State the preparation type.
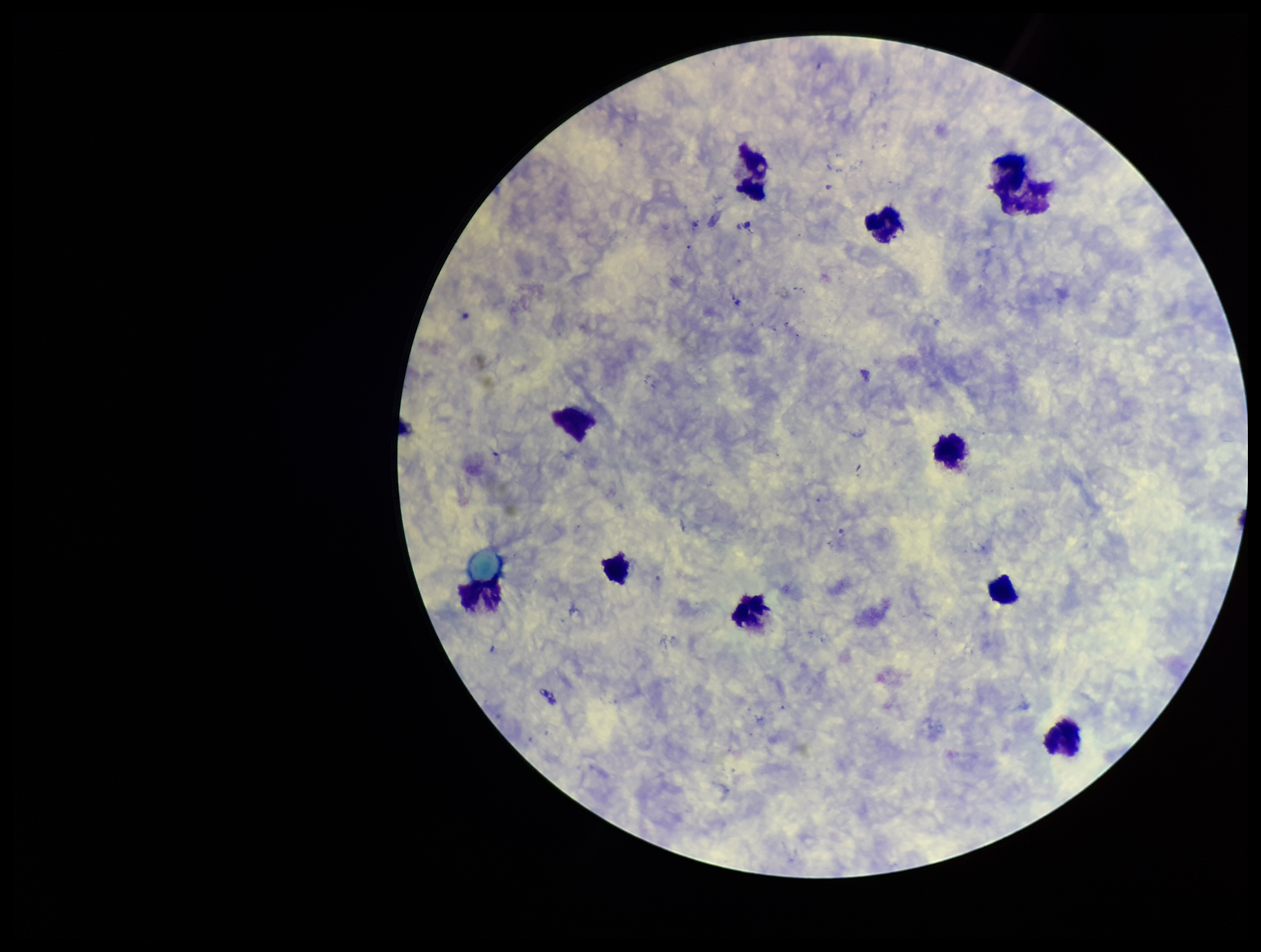
It is a thick blood smear.

image size = 1261×952 pixels
field of view = one from this slide
leukocyte count = 10
stain = Giemsa
Plasmodium parasites = none detected
capture = smartphone photograph through the microscope eyepiece
patient malaria status = negative
parasite count = 0